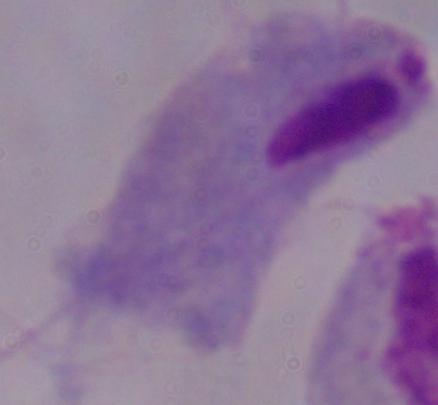
identification = trichomonad
magnification = 1000x
modality = micrograph